Point out each malaria parasite.
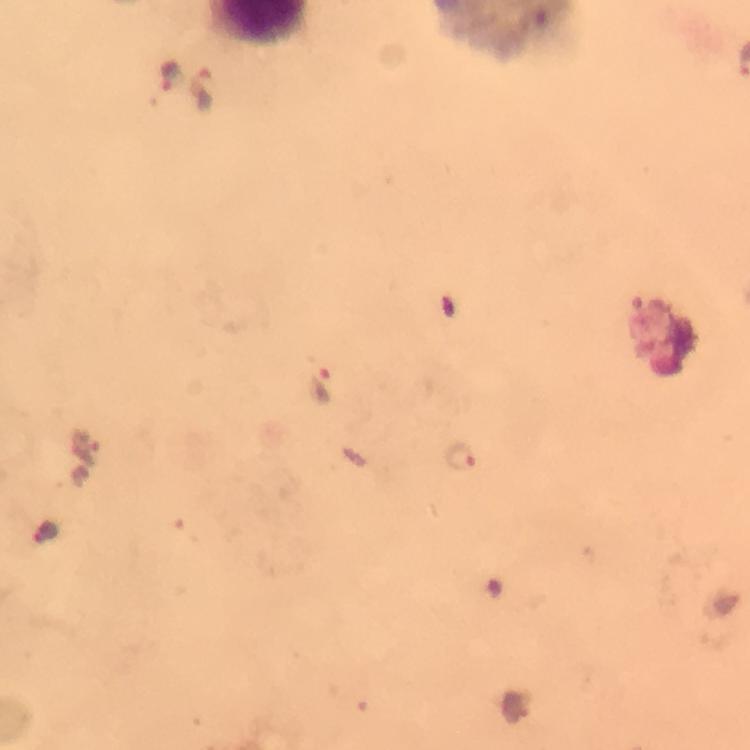
Approximate centers as {x, y} in pixels.
Malaria parasites: {173, 77}, {203, 89}, {320, 386}, {89, 446}, {460, 455}.

{
  "capture": "smartphone mounted on the microscope",
  "cropped_from": "one field of view",
  "immersion_oil": "used",
  "magnification": "100x",
  "image_size": "750×750 pixels",
  "preparation": "thick smear",
  "stain": "Giemsa",
  "context": "from a malaria diagnostic workup"
}